Classify this cell by malaria status.
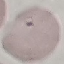
It is uninfected.

Summary:
  - Capture: smartphone through the microscope eyepiece
  - Stain: Giemsa
  - Preparation: thin smear
  - Image type: cell patch, automatically extracted from a larger field of view and resized to 64 × 64 pixels